Identify the parasite.
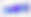

Toxoplasma gondii.

modality: micrograph
magnification: 400x